State the blood parasite species.
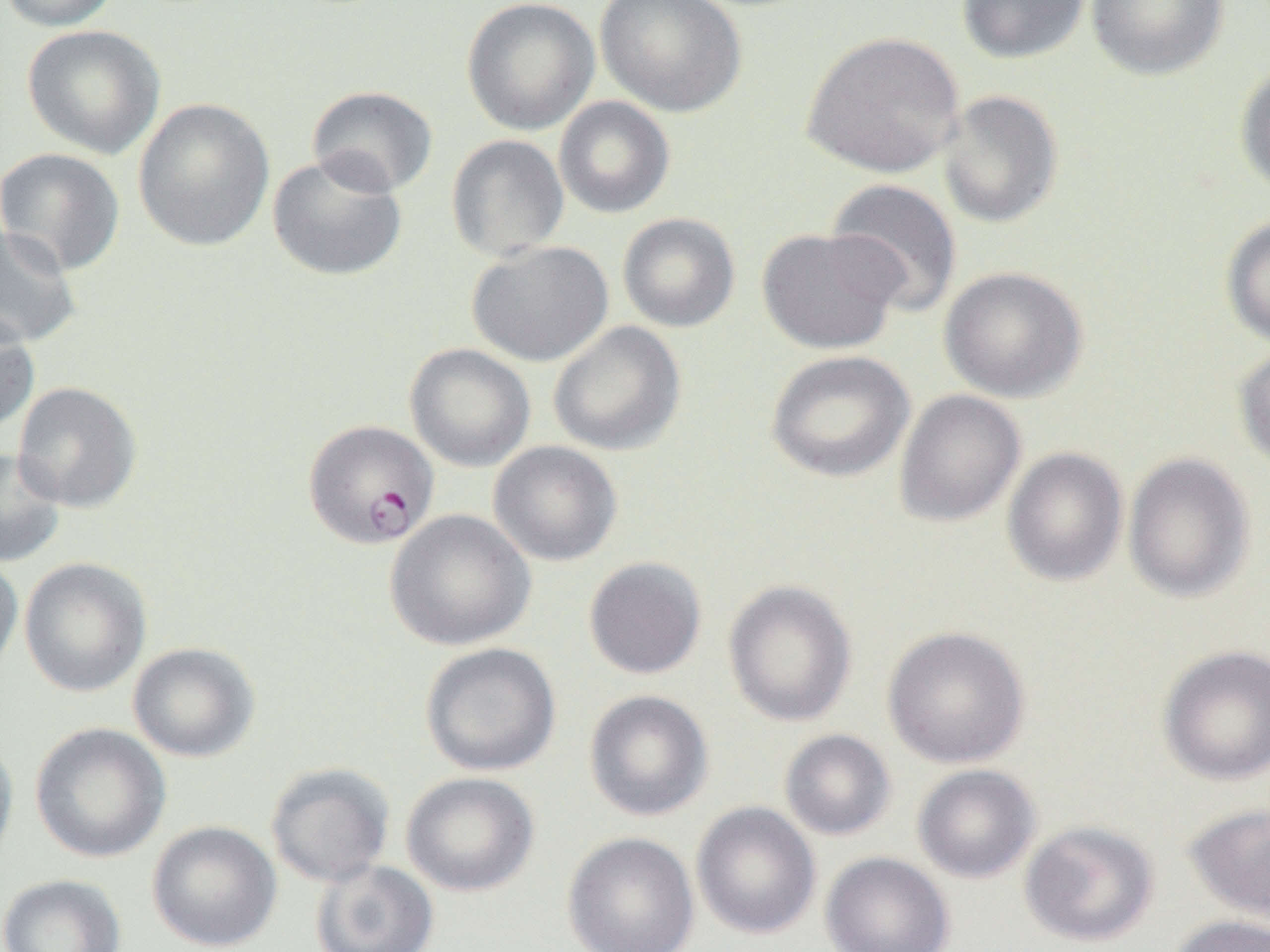
Plasmodium falciparum.

Summary:
  - Coordinate format: approximate bounding boxes as named x1/y1/x2/y2 corners in pixels
  - Uninfected red blood cell locations: (x1=0, y1=0, x2=121, y2=31), (x1=461, y1=0, x2=600, y2=136), (x1=596, y1=0, x2=746, y2=118), (x1=956, y1=0, x2=1091, y2=65), (x1=1086, y1=0, x2=1229, y2=81), (x1=22, y1=24, x2=165, y2=159), (x1=801, y1=31, x2=965, y2=179), (x1=1234, y1=60, x2=1270, y2=196), (x1=306, y1=85, x2=438, y2=197), (x1=937, y1=89, x2=1064, y2=229), (x1=553, y1=96, x2=675, y2=219), (x1=132, y1=97, x2=275, y2=253), (x1=446, y1=134, x2=570, y2=261), (x1=0, y1=147, x2=126, y2=277), (x1=268, y1=152, x2=408, y2=282), (x1=824, y1=178, x2=962, y2=317), (x1=617, y1=212, x2=740, y2=333), (x1=1220, y1=214, x2=1270, y2=349), (x1=0, y1=225, x2=82, y2=349), (x1=756, y1=227, x2=903, y2=354), (x1=467, y1=240, x2=613, y2=367), (x1=939, y1=266, x2=1088, y2=404), (x1=0, y1=310, x2=40, y2=437), (x1=548, y1=320, x2=687, y2=456), (x1=1233, y1=340, x2=1270, y2=473), (x1=405, y1=343, x2=535, y2=472), (x1=765, y1=350, x2=915, y2=483), (x1=12, y1=381, x2=142, y2=513), (x1=893, y1=389, x2=1026, y2=528), (x1=488, y1=441, x2=623, y2=567), (x1=0, y1=447, x2=66, y2=567), (x1=1002, y1=447, x2=1129, y2=586), (x1=1123, y1=451, x2=1256, y2=603), (x1=385, y1=509, x2=535, y2=651), (x1=0, y1=551, x2=24, y2=684), (x1=583, y1=556, x2=707, y2=679), (x1=19, y1=558, x2=152, y2=697), (x1=722, y1=579, x2=858, y2=727), (x1=882, y1=625, x2=1031, y2=769), (x1=127, y1=642, x2=260, y2=762), (x1=420, y1=642, x2=561, y2=777), (x1=1157, y1=645, x2=1270, y2=786), (x1=584, y1=689, x2=713, y2=822), (x1=29, y1=722, x2=171, y2=863), (x1=779, y1=729, x2=896, y2=841), (x1=0, y1=733, x2=19, y2=874), (x1=265, y1=762, x2=395, y2=887), (x1=912, y1=764, x2=1041, y2=884), (x1=401, y1=772, x2=540, y2=896), (x1=691, y1=801, x2=821, y2=940), (x1=1184, y1=802, x2=1270, y2=922), (x1=147, y1=820, x2=282, y2=951), (x1=1019, y1=820, x2=1160, y2=948), (x1=562, y1=832, x2=700, y2=952), (x1=819, y1=851, x2=955, y2=952), (x1=310, y1=859, x2=439, y2=952), (x1=0, y1=873, x2=126, y2=952), (x1=1166, y1=914, x2=1270, y2=952)
  - Plasmodium falciparum-infected red blood cell locations: (x1=303, y1=419, x2=440, y2=550)
  - Preparation: thin blood film
  - Modality: optical microscopy
  - Field of view: single
  - Image size: 1270×952 pixels
  - Magnification: 1000x